Evaluate for Plasmodium parasites.
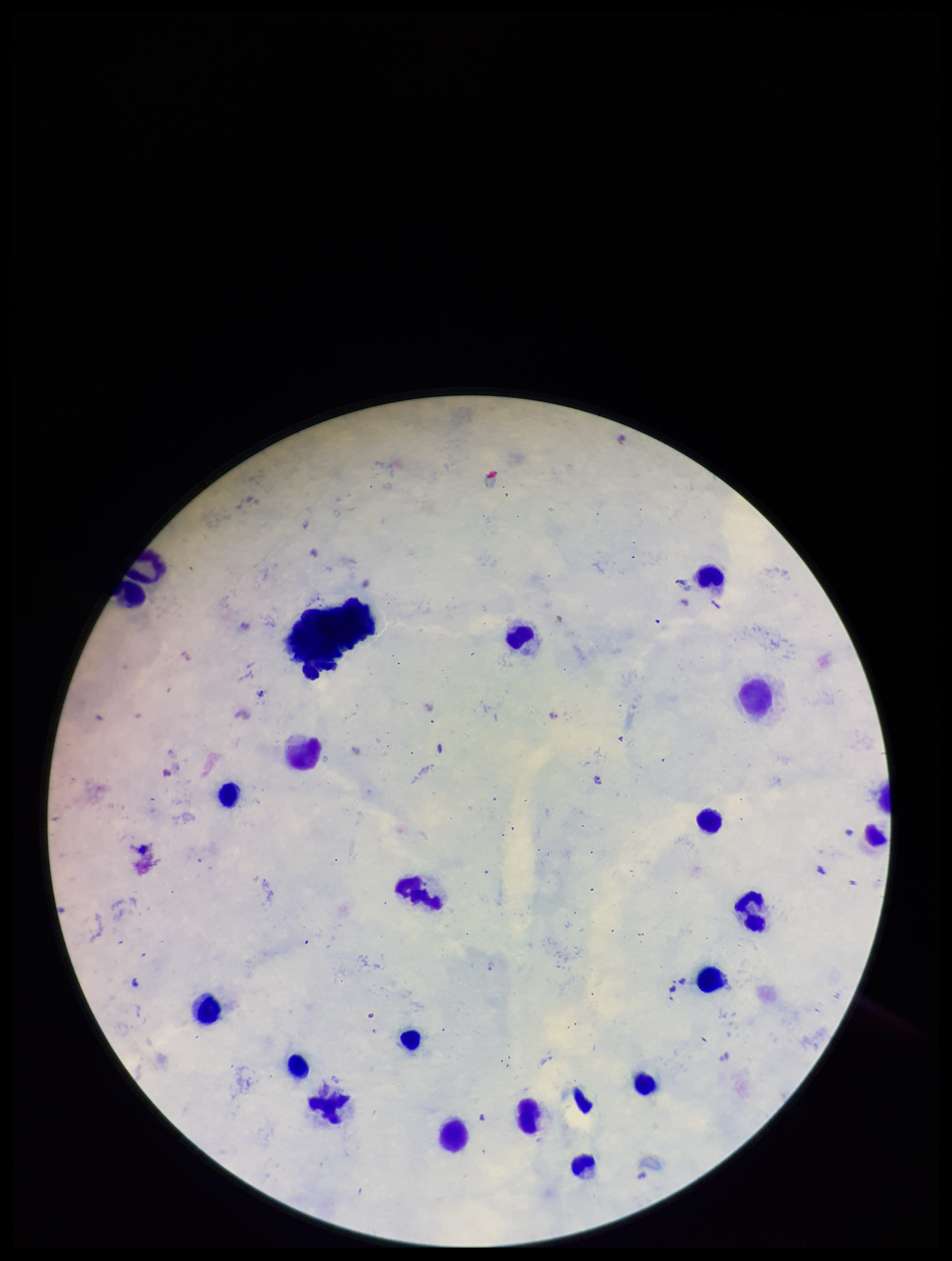
Identified.

patient malaria status = positive
parasite count = 4
species reported for this patient = Plasmodium falciparum
preparation = thick smear
capture = smartphone photograph through the microscope eyepiece
image size = 952×1261 pixels
stain = Giemsa
leukocyte count = 19
field of view = one from this slide